Report the malaria status of this cell.
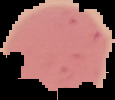
It is uninfected.

Image is 115×100 pixels. The area outside the segmented cell region is set to black. From a thin blood smear.